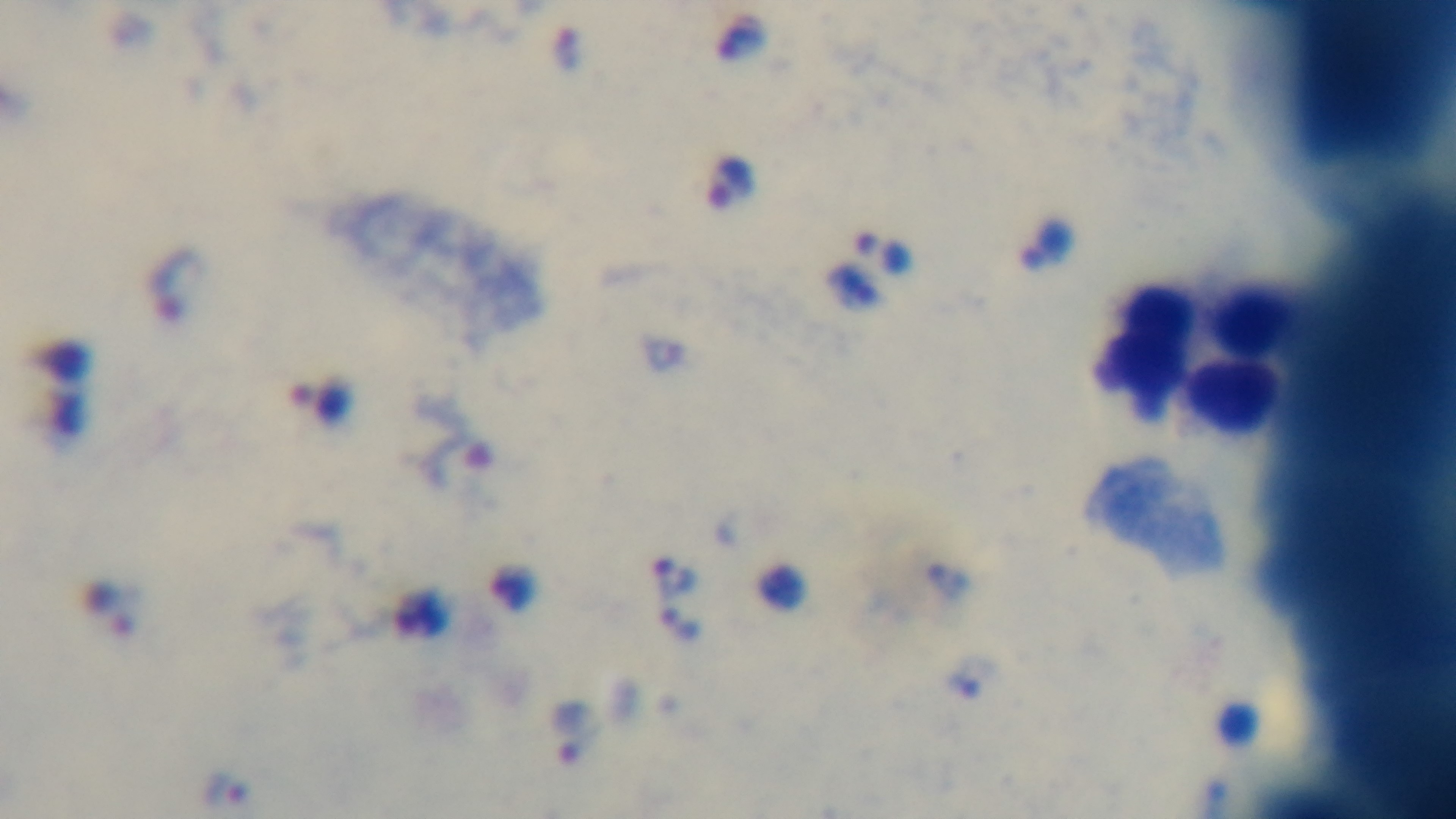

Summary:
  - Malaria status: positive
  - Field of view: one from the slide
  - Modality: light microscopy
  - Stain: Giemsa
  - Objective: 100x oil immersion
  - Capture: mounted 4K digital camera
  - Preparation: thick